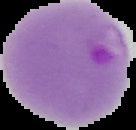
malaria status = parasitized
image type = cell region segmented out of the field of view; surrounding area masked to black
preparation = thin blood smear
image size = 136×130 pixels